Locate every Plasmodium parasite.
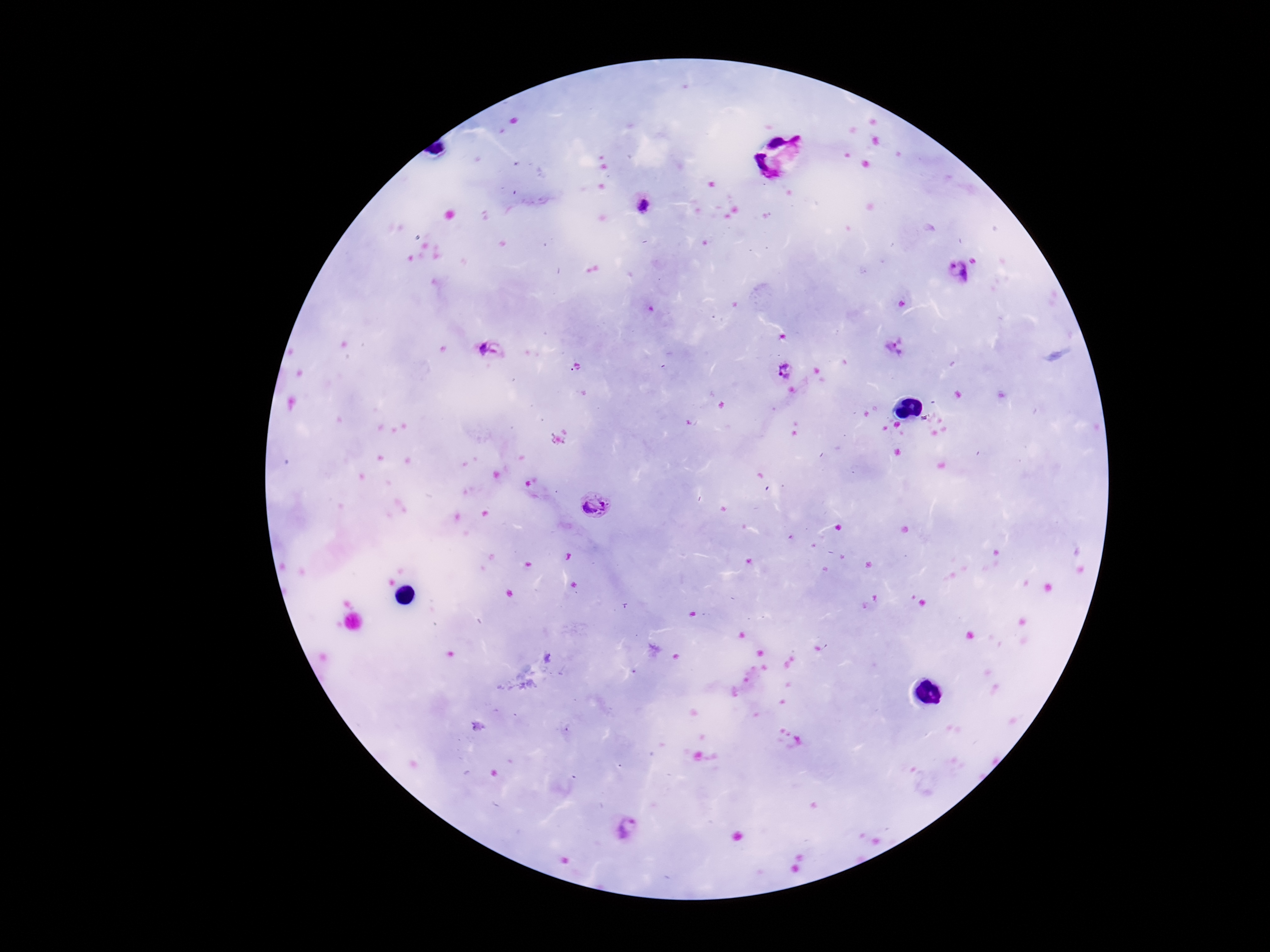
Approximate centers as (x, y) in pixels.
Plasmodium parasites: (642, 205), (956, 272), (897, 346), (492, 350), (785, 369), (596, 504), (627, 829).

Patient malaria status: positive. Thick blood film. Giemsa-stained preparation. Single field of view. Smartphone photograph taken through the microscope eyepiece. 100x magnification. Image is 1270×952 pixels.